State the preparation type.
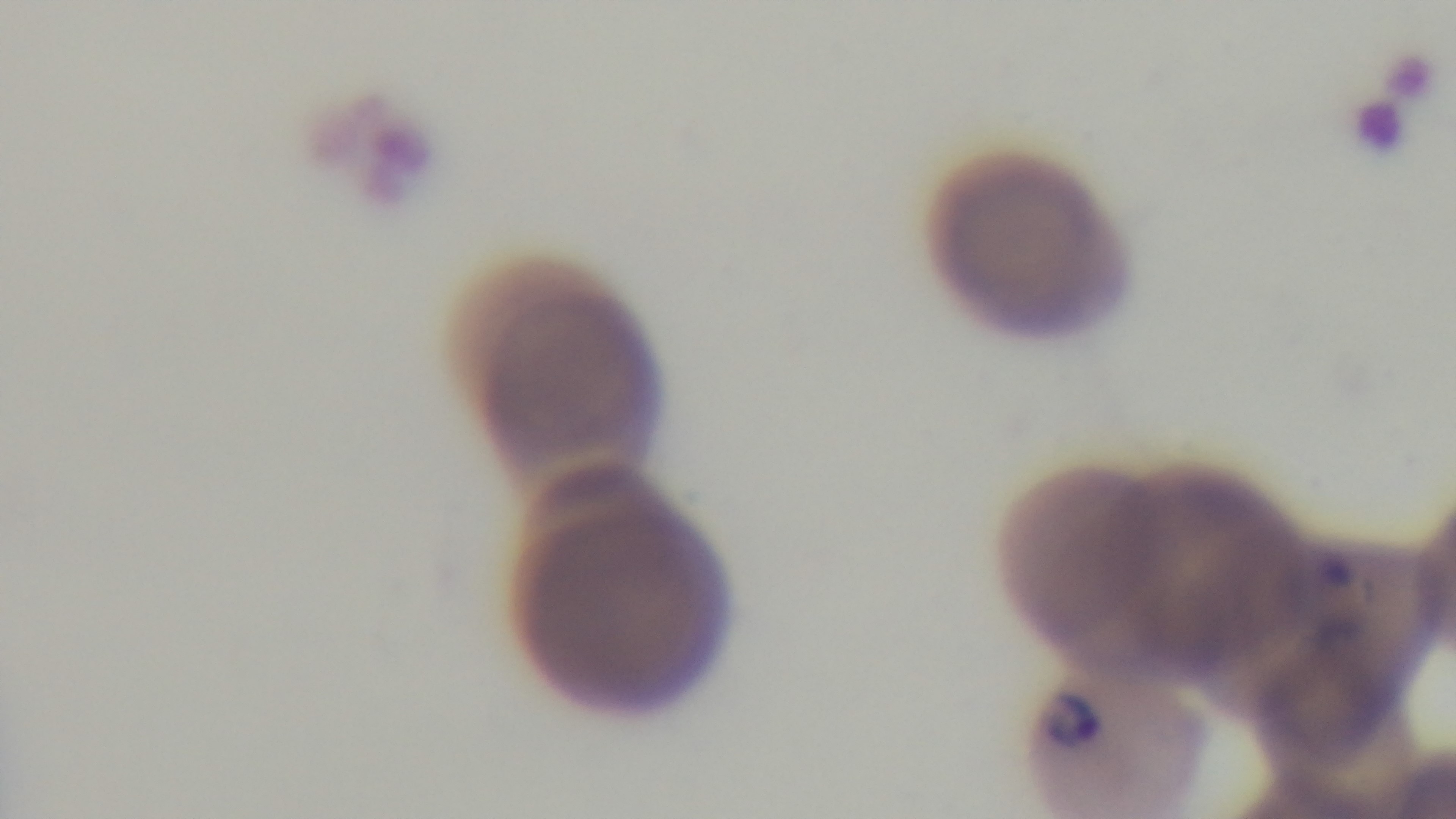

It is a thin blood film.

Summary:
  - Objective: 100x oil immersion
  - Capture: mounted 4K digital camera
  - Modality: light microscopy
  - Malaria status: positive
  - Field of view: single
  - Stain: Giemsa